Comment on the morphology of the red blood cells.
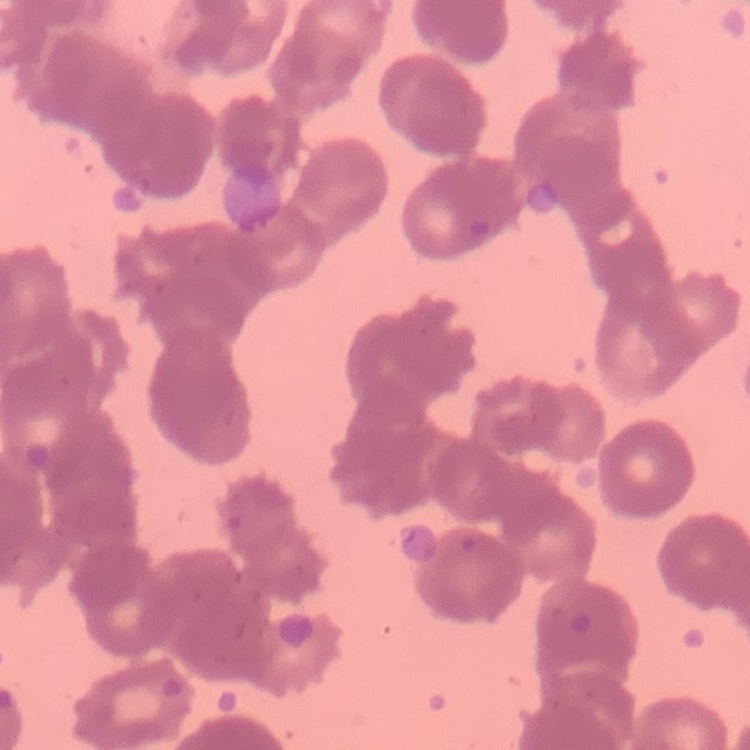

Rouleaux formation.

preparation = thin blood smear
stain = Field's or Giemsa
image type = square crop of a larger photomicrograph